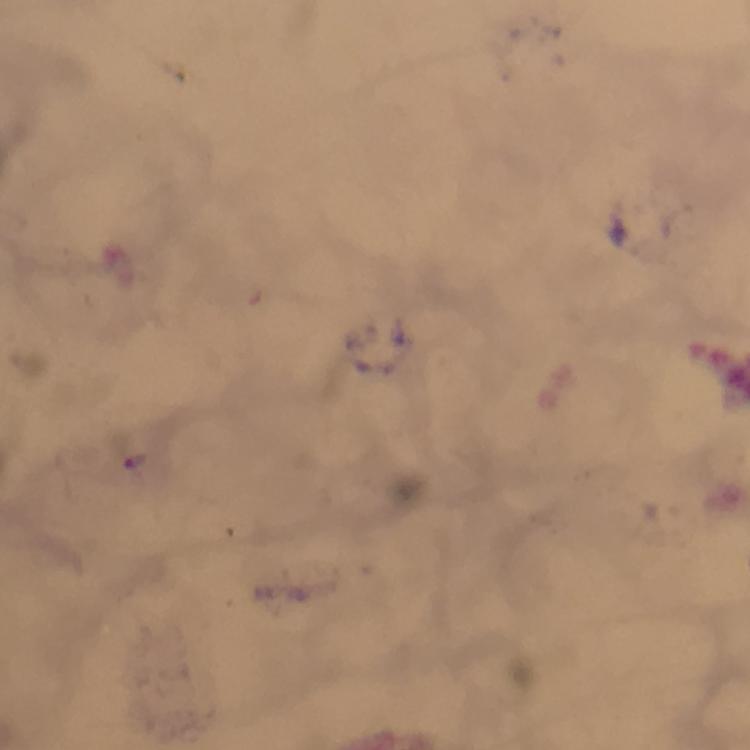
Approximate centers as [x, y] in pixels.
Summary:
  - Plasmodium parasite locations: [137, 461]
  - Immersion oil: applied
  - Cropped from: a single field of view
  - Context: from a malaria diagnostic workup
  - Image size: 750×750 pixels
  - Magnification: 100x
  - Capture: smartphone photograph through a microscope
  - Preparation: thick blood film
  - Stain: Giemsa